Locate every malaria parasite.
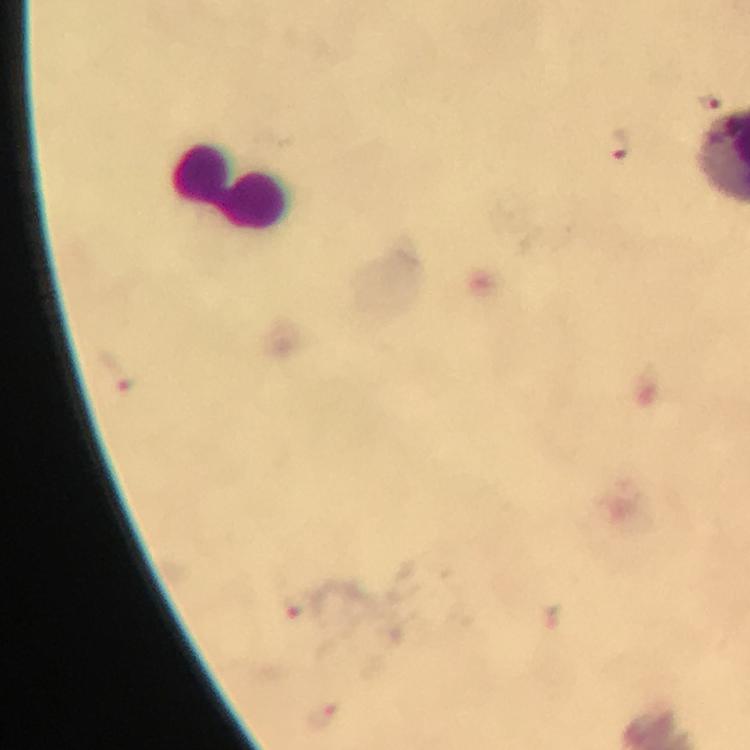

Approximate object centers, in pixels from the top-left corner.
Malaria parasites: (x=711, y=103), (x=617, y=144), (x=117, y=373), (x=299, y=608), (x=549, y=619), (x=321, y=717).

Summary:
  - Leukocyte locations: (x=231, y=185)
  - Preparation: thick smear
  - Context: from a malaria diagnostic workup
  - Image size: 750×750 pixels
  - Cropped from: a single field of view
  - Immersion oil: used
  - Magnification: 100x
  - Stain: Giemsa
  - Capture: smartphone camera through the microscope